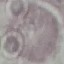

{
  "result": "no malaria parasites seen",
  "preparation": "thin blood film",
  "image_type": "automatically extracted cell patch, resized to 64 × 64 pixels",
  "stain": "Giemsa",
  "capture": "smartphone through the microscope eyepiece"
}